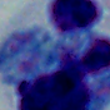

identification = white blood cell
modality = micrograph
magnification = 1000x